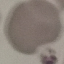
result: no malaria parasites seen
capture: smartphone camera at the microscope eyepiece
stain: Giemsa
preparation: thin smear
image_type: cell patch, automatically extracted from a larger field of view and resized to 64 × 64 pixels